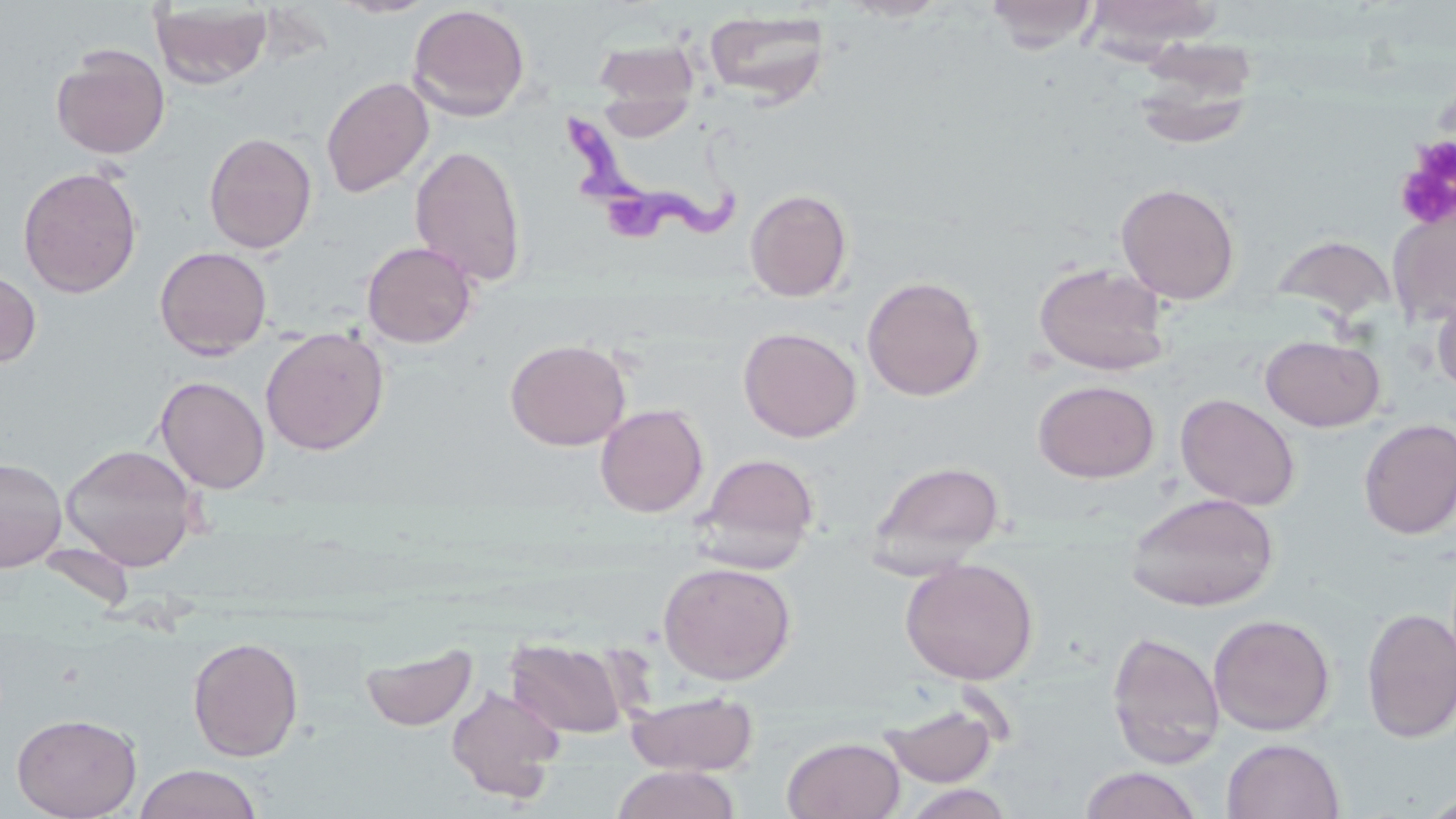

Summary:
  - Coordinate format: approximate bounding boxes as named x1/y1/x2/y2 corners in pixels
  - Trypanosoma brucei locations: (x1=566, y1=110, x2=751, y2=251)
  - Uninfected red blood cell locations: (x1=330, y1=0, x2=439, y2=18), (x1=839, y1=0, x2=952, y2=22), (x1=985, y1=0, x2=1099, y2=54), (x1=1080, y1=0, x2=1224, y2=59), (x1=149, y1=2, x2=275, y2=89), (x1=407, y1=4, x2=531, y2=121), (x1=702, y1=9, x2=832, y2=105), (x1=592, y1=38, x2=701, y2=114), (x1=1131, y1=42, x2=1259, y2=151), (x1=50, y1=44, x2=171, y2=159), (x1=321, y1=76, x2=434, y2=198), (x1=203, y1=131, x2=318, y2=254), (x1=409, y1=143, x2=528, y2=288), (x1=18, y1=165, x2=143, y2=298), (x1=1115, y1=182, x2=1241, y2=305), (x1=745, y1=188, x2=853, y2=302), (x1=1387, y1=202, x2=1456, y2=326), (x1=1273, y1=233, x2=1396, y2=324), (x1=361, y1=241, x2=479, y2=349), (x1=154, y1=246, x2=272, y2=359), (x1=1033, y1=261, x2=1172, y2=376), (x1=0, y1=266, x2=41, y2=369), (x1=861, y1=275, x2=985, y2=402), (x1=1431, y1=287, x2=1456, y2=398), (x1=260, y1=326, x2=389, y2=455), (x1=738, y1=327, x2=862, y2=443), (x1=1260, y1=335, x2=1385, y2=432), (x1=505, y1=338, x2=631, y2=451), (x1=155, y1=375, x2=270, y2=494), (x1=1033, y1=380, x2=1160, y2=483), (x1=1175, y1=393, x2=1300, y2=510), (x1=595, y1=403, x2=709, y2=518), (x1=1357, y1=418, x2=1456, y2=540), (x1=60, y1=442, x2=202, y2=572), (x1=694, y1=453, x2=820, y2=571), (x1=0, y1=457, x2=67, y2=571), (x1=867, y1=459, x2=1007, y2=572), (x1=1125, y1=491, x2=1280, y2=612), (x1=900, y1=557, x2=1039, y2=685), (x1=658, y1=561, x2=797, y2=685), (x1=1360, y1=607, x2=1456, y2=744), (x1=1208, y1=613, x2=1335, y2=736), (x1=1106, y1=630, x2=1226, y2=770), (x1=188, y1=637, x2=304, y2=762), (x1=505, y1=637, x2=628, y2=739), (x1=361, y1=643, x2=478, y2=732), (x1=446, y1=685, x2=566, y2=803), (x1=625, y1=690, x2=758, y2=776), (x1=879, y1=699, x2=1002, y2=787), (x1=11, y1=711, x2=142, y2=819), (x1=782, y1=736, x2=905, y2=819), (x1=1222, y1=738, x2=1345, y2=819), (x1=133, y1=764, x2=264, y2=819), (x1=610, y1=765, x2=742, y2=819), (x1=1078, y1=766, x2=1205, y2=819), (x1=901, y1=783, x2=1016, y2=819)
  - Platelet locations: (x1=1393, y1=137, x2=1456, y2=231)
  - Slide-level diagnosis: Trypanosoma brucei
  - Stain: May-Grünwald-Giemsa
  - Modality: optical microscopy
  - Field of view: one of a larger specimen
  - Preparation: thin blood smear
  - Image size: 1456×819 pixels
  - Magnification: 1000x